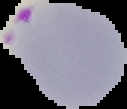

Segmented cell region on a black background. Image is 127×109 pixels. Result: Plasmodium parasites detected. From a thin blood film.